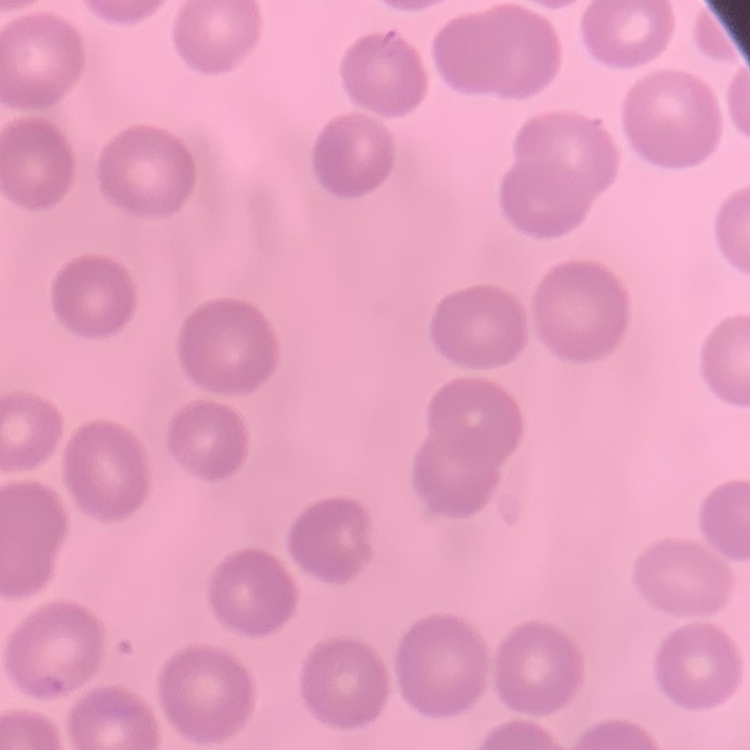

Summary:
  - Red blood cell morphology: no rouleaux formation
  - Stain: Field's or Giemsa
  - Image type: one tile cut from a larger photomicrograph
  - Preparation: thin blood film